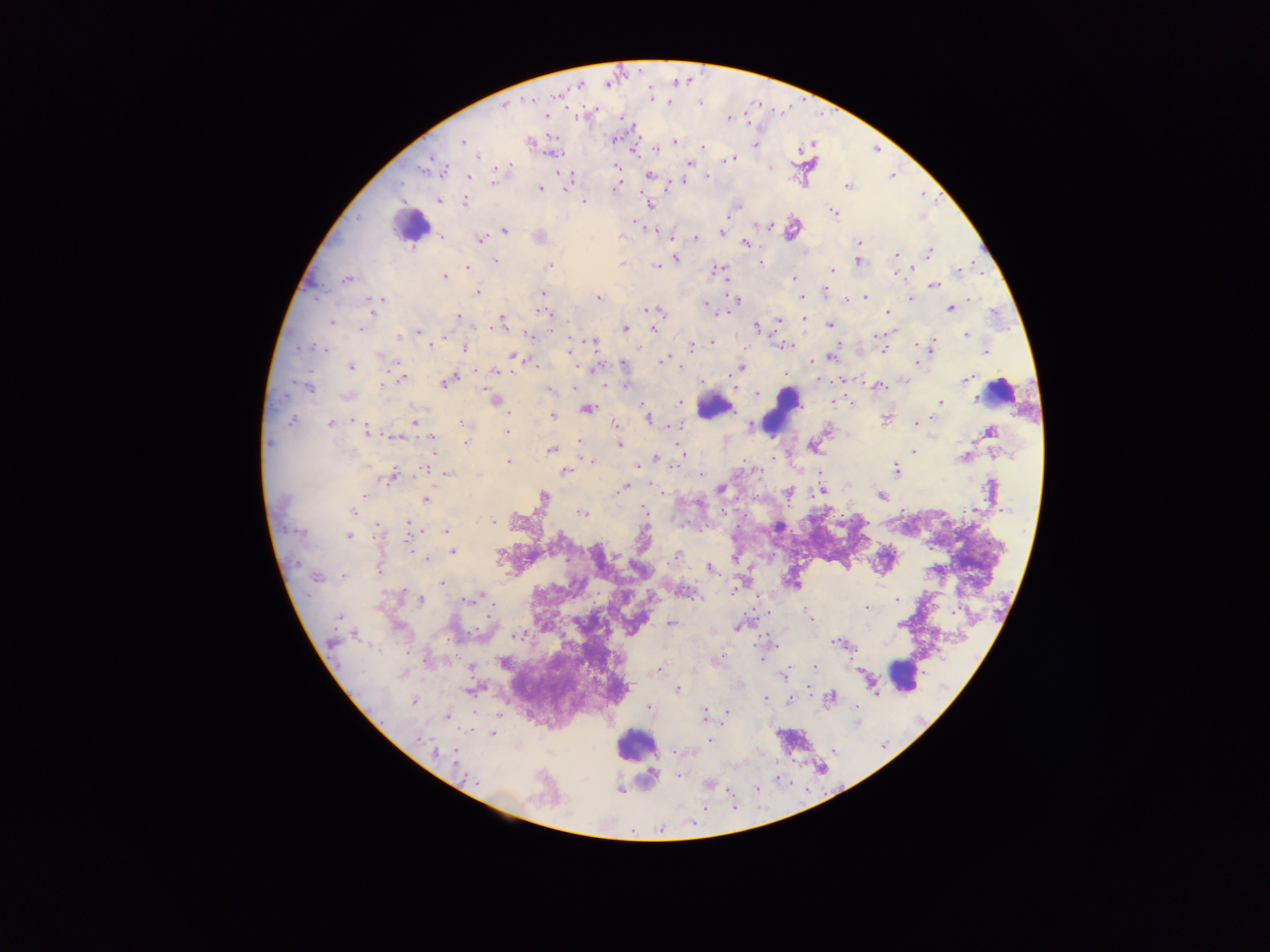

Approximate centers as {x, y} in pixels.
Summary:
  - Leukocyte locations: {410, 226}, {999, 392}, {715, 407}, {783, 411}, {903, 676}, {637, 745}
  - Plasmodium parasite locations: {638, 69}, {675, 79}, {687, 79}, {583, 81}, {607, 83}, {649, 87}, {569, 88}, {580, 88}, {560, 94}, {531, 99}, {651, 100}, {803, 100}, {670, 101}, {701, 102}, {761, 103}, {790, 103}, {504, 106}, {566, 106}, {583, 107}, {596, 107}, {774, 109}, {837, 110}, {744, 111}, {620, 113}, {783, 113}, {545, 114}, {821, 116}, {728, 118}, {750, 121}, {632, 124}, {641, 135}, {423, 138}, {614, 139}, {528, 140}, {462, 141}, {635, 142}, {674, 143}, {756, 145}, {654, 146}, {703, 147}, {797, 147}, {881, 148}, {630, 150}, {553, 152}, {639, 155}, {478, 156}, {728, 158}, {431, 159}, {688, 163}, {510, 164}, {496, 167}, {615, 167}, {417, 170}, {443, 173}, {649, 173}, {563, 175}, {895, 175}, {708, 176}, {468, 177}, {685, 180}, {402, 183}, {492, 184}, {565, 185}, {846, 185}, {540, 187}, {666, 187}, {615, 188}, {641, 193}, {942, 193}, {925, 194}, {934, 199}, {438, 201}, {464, 201}, {583, 201}, {648, 204}, {730, 212}, {832, 212}, {358, 215}, {631, 221}, {761, 224}, {645, 225}, {766, 225}, {792, 228}, {657, 229}, {505, 231}, {719, 232}, {539, 235}, {441, 236}, {480, 237}, {670, 237}, {695, 237}, {859, 242}, {744, 243}, {929, 252}, {895, 255}, {675, 257}, {495, 260}, {857, 260}, {973, 262}, {760, 263}, {622, 264}, {550, 265}, {655, 265}, {467, 267}, {910, 268}, {720, 270}, {830, 271}, {894, 272}, {957, 272}, {982, 273}, {444, 276}, {724, 277}, {794, 278}, {346, 279}, {933, 284}, {477, 292}, {824, 292}, {542, 293}, {315, 296}, {598, 297}, {801, 297}, {380, 298}, {865, 298}, {734, 299}, {844, 299}, {909, 299}, {969, 300}, {704, 304}, {950, 307}, {371, 308}, {651, 310}, {541, 311}, {726, 312}, {887, 312}, {458, 316}, {778, 319}, {804, 319}, {502, 320}, {330, 322}, {830, 324}, {757, 326}, {490, 327}, {624, 327}, {654, 327}, {474, 328}, {360, 329}, {552, 329}, {887, 331}, {418, 332}, {528, 334}, {875, 334}, {569, 335}, {966, 335}, {399, 336}, {444, 337}, {769, 338}, {591, 341}, {314, 343}, {712, 343}, {931, 343}, {837, 344}, {430, 345}, {785, 345}, {693, 346}, {916, 346}, {465, 348}, {883, 349}, {300, 350}, {326, 351}, {568, 351}, {932, 351}, {986, 351}, {513, 354}, {832, 354}, {662, 359}, {813, 362}, {919, 362}, {399, 363}, {533, 364}, {622, 364}, {351, 367}, {741, 367}, {476, 368}, {680, 368}, {594, 369}, {388, 370}, {495, 370}, {313, 371}, {785, 375}, {402, 378}, {450, 379}, {819, 379}, {967, 379}, {844, 380}, {831, 381}, {294, 382}, {863, 382}, {382, 384}, {626, 384}, {733, 385}, {879, 386}, {307, 387}, {574, 387}, {486, 388}, {550, 391}, {757, 393}, {289, 394}, {346, 396}, {494, 399}, {832, 399}, {641, 401}, {851, 401}, {940, 402}, {679, 403}, {586, 408}, {509, 412}, {552, 415}, {933, 417}, {647, 418}, {886, 418}, {354, 419}, {291, 420}, {329, 422}, {414, 422}, {915, 423}, {463, 424}, {615, 425}, {673, 425}, {750, 426}, {369, 430}, {826, 430}, {989, 431}, {506, 433}, {396, 436}, {417, 437}, {432, 439}, {269, 442}, {465, 442}, {579, 443}, {620, 444}, {676, 446}, {813, 446}, {551, 450}, {913, 451}, {433, 453}, {684, 454}, {965, 457}, {655, 458}, {745, 459}, {771, 460}, {590, 461}, {508, 462}, {637, 465}, {673, 468}, {427, 469}, {565, 471}, {896, 471}, {439, 472}, {445, 472}, {700, 474}, {821, 474}, {392, 475}, {649, 484}, {625, 487}, {720, 489}, {821, 491}, {663, 493}, {788, 493}, {363, 494}, {881, 495}, {757, 496}, {543, 497}, {986, 498}, {426, 499}, {721, 508}, {644, 509}, {903, 509}, {1001, 509}, {353, 511}, {972, 511}, {582, 513}, {843, 513}, {745, 517}, {493, 519}, {706, 522}, {869, 523}, {408, 524}, {378, 526}, {683, 526}, {738, 527}, {409, 530}, {421, 530}, {446, 530}, {301, 532}, {700, 533}, {348, 536}, {373, 536}, {932, 549}, {453, 551}, {413, 552}, {773, 554}, {677, 555}, {734, 556}, {426, 558}, {378, 566}, {707, 566}, {343, 576}, {316, 577}, {442, 583}, {792, 584}, {680, 586}, {404, 589}, {734, 590}, {759, 594}, {478, 595}, {421, 599}, {468, 599}, {700, 599}, {896, 600}, {495, 602}, {868, 607}, {752, 608}, {766, 613}, {952, 613}, {487, 616}, {338, 617}, {754, 619}, {810, 619}, {670, 624}, {900, 624}, {738, 626}, {478, 628}, {470, 632}, {759, 633}, {353, 634}, {767, 634}, {515, 635}, {447, 639}, {332, 642}, {839, 643}, {755, 644}, {779, 646}, {856, 648}, {409, 654}, {851, 658}, {716, 659}, {424, 660}, {762, 660}, {503, 662}, {787, 666}, {813, 668}, {659, 670}, {474, 675}, {784, 675}, {808, 687}, {627, 688}, {472, 689}, {677, 689}, {810, 692}, {831, 697}, {765, 698}, {789, 700}, {414, 701}, {856, 703}, {649, 708}, {726, 711}, {475, 712}, {704, 714}, {723, 714}, {447, 716}, {383, 721}, {492, 734}, {418, 738}, {710, 740}, {882, 746}, {835, 750}, {674, 752}, {435, 753}, {455, 755}, {456, 761}, {678, 775}, {621, 789}, {729, 791}, {735, 808}, {709, 810}, {691, 824}, {662, 830}
  - Preparation: thick blood smear
  - Field of view: single
  - Capture: mobile-phone photograph through a microscope
  - Image size: 1270×952 pixels
  - Country: Ghana